Classify this cell by malaria status.
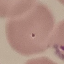

It is parasitized.

image type = automatically extracted cell patch, resized to 64 × 64 pixels
capture = smartphone camera at the microscope eyepiece
preparation = thin smear
stain = Giemsa